Mark where leukocytes are.
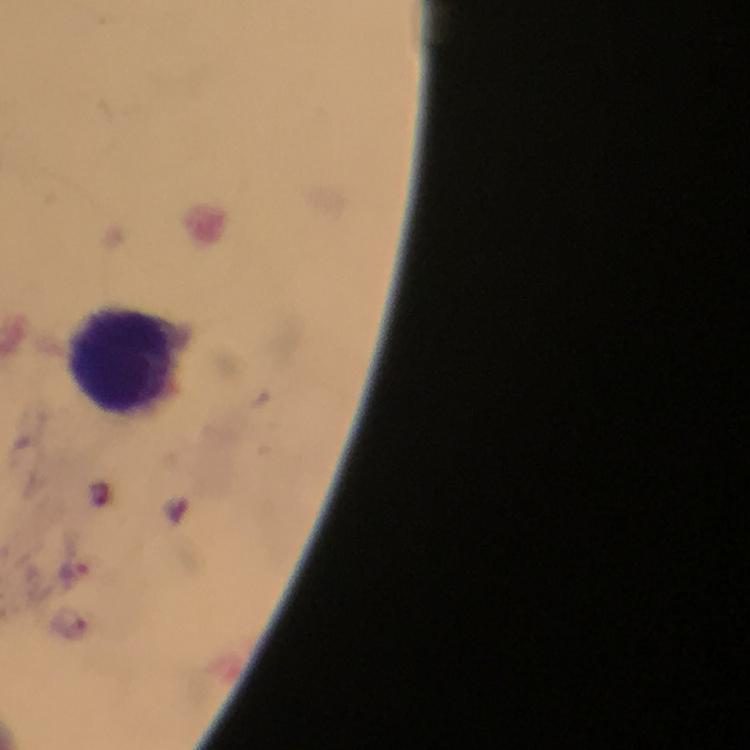
Approximate centers as (x, y) in pixels.
Leukocytes: (121, 361).

Plasmodium parasite locations: (99, 494), (75, 573), (71, 624). From a diagnostic examination for malaria. Cropped region of a single field of view. 100x magnification. Smartphone photograph taken through a microscope. Giemsa stain. Thick smear. Immersion oil was used. Image is 750×750 pixels.